Assess this cell for malaria.
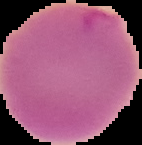
Uninfected.

image_size: 142×145 pixels
preparation: thin blood film
image_type: segmented cell region with the area outside set to black